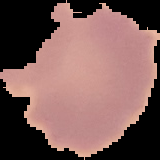
From a thin blood film. Malaria status: uninfected. Image is 160×160 pixels. Cell region segmented out of the field of view; the surrounding area is masked to black.